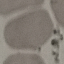
result = no malaria parasites detected
capture = smartphone camera at the microscope eyepiece
image type = automatically extracted cell patch, resized to 64 × 64 pixels
stain = Giemsa
preparation = thin blood film